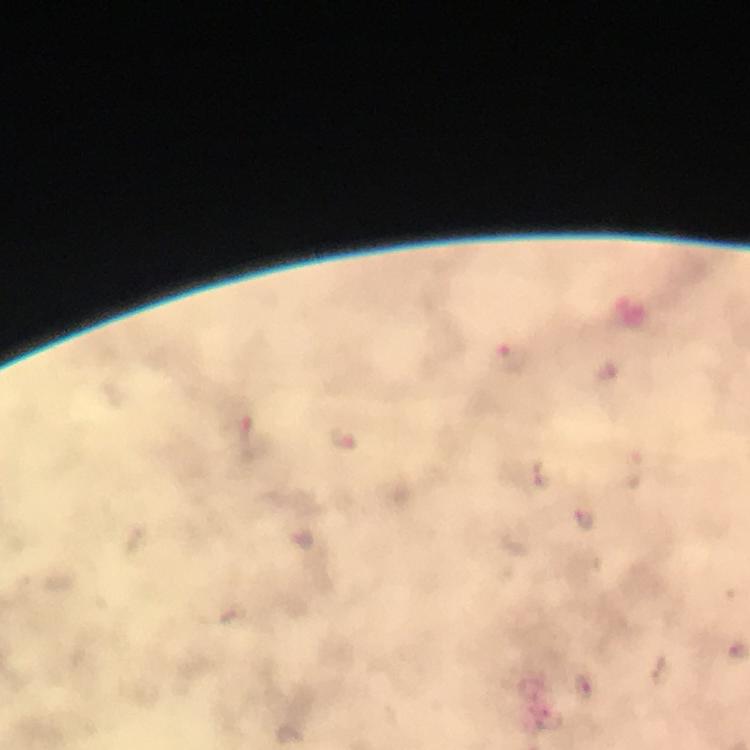

Approximate object centers, in pixels from the top-left corner.
Summary:
  - Malaria parasite locations: (x=515, y=358), (x=252, y=438), (x=344, y=438), (x=585, y=521)
  - Cropped from: one field of view
  - Image size: 750×750 pixels
  - Magnification: 100x
  - Context: from a diagnostic examination for malaria
  - Capture: smartphone mounted on the microscope
  - Stain: Giemsa
  - Preparation: thick blood smear
  - Immersion oil: used